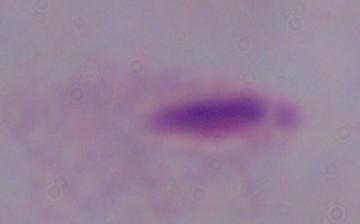

Micrograph. Captured at 1000x magnification. A trichomonad is seen.